Classify this cell by malaria status.
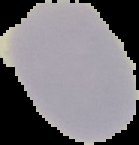
Uninfected.

image size = 139×145 pixels
image type = segmented cell region with the area outside set to black
preparation = thin blood film